Name the parasite shown.
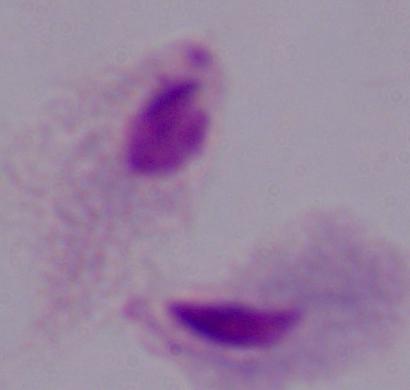
A trichomonad.

magnification = 1000x
modality = photomicrograph